Assess this cell for malaria.
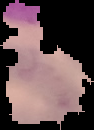

It is uninfected.

Summary:
  - Preparation: thin blood film
  - Image size: 94×130 pixels
  - Image type: segmented cell region with the area outside set to black